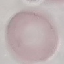
malaria status = uninfected
image type = cell patch, automatically extracted from a larger field of view and resized to 64 × 64 pixels
preparation = thin blood film
stain = Giemsa
capture = smartphone camera at the microscope eyepiece